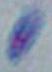
Summary:
  - Magnification: 1000x
  - Modality: micrograph
  - Identification: Toxoplasma gondii